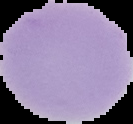

Summary:
  - Preparation: thin blood film
  - Malaria status: uninfected
  - Image size: 133×124 pixels
  - Image type: cell region segmented out of the field of view; surrounding area masked to black